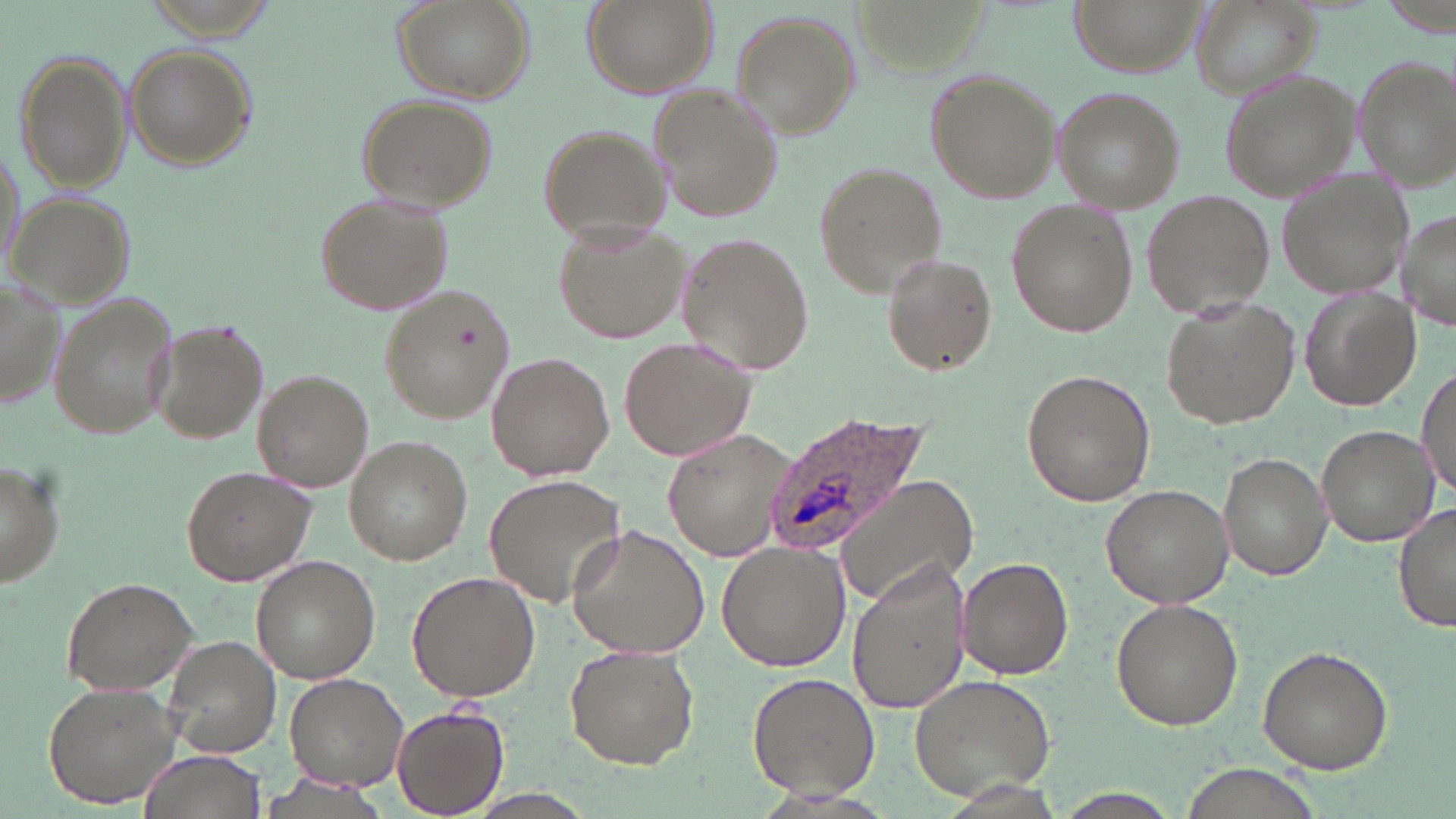
Summary:
  - Coordinate format: approximate bounding boxes as named x1/y1/x2/y2 corners in pixels
  - Plasmodium ovale-infected red blood cell locations: (x1=765, y1=411, x2=934, y2=553)
  - Uninfected red blood cell locations: (x1=391, y1=0, x2=535, y2=103), (x1=580, y1=0, x2=717, y2=99), (x1=1076, y1=0, x2=1205, y2=74), (x1=1189, y1=0, x2=1322, y2=101), (x1=729, y1=10, x2=858, y2=135), (x1=125, y1=43, x2=256, y2=172), (x1=16, y1=52, x2=132, y2=194), (x1=1353, y1=52, x2=1455, y2=188), (x1=922, y1=68, x2=1060, y2=203), (x1=1219, y1=71, x2=1357, y2=202), (x1=651, y1=86, x2=783, y2=223), (x1=1056, y1=89, x2=1182, y2=210), (x1=356, y1=95, x2=497, y2=211), (x1=535, y1=124, x2=669, y2=246), (x1=814, y1=162, x2=947, y2=294), (x1=1278, y1=170, x2=1413, y2=298), (x1=313, y1=189, x2=454, y2=316), (x1=1143, y1=189, x2=1275, y2=320), (x1=7, y1=191, x2=135, y2=310), (x1=1005, y1=199, x2=1136, y2=339), (x1=1398, y1=205, x2=1456, y2=332), (x1=553, y1=219, x2=690, y2=345), (x1=677, y1=233, x2=814, y2=372), (x1=882, y1=253, x2=995, y2=374), (x1=0, y1=276, x2=65, y2=414), (x1=378, y1=283, x2=517, y2=424), (x1=1300, y1=286, x2=1420, y2=411), (x1=48, y1=292, x2=179, y2=441), (x1=1160, y1=298, x2=1298, y2=428), (x1=149, y1=318, x2=270, y2=444), (x1=619, y1=335, x2=755, y2=462), (x1=487, y1=353, x2=615, y2=480), (x1=1416, y1=366, x2=1455, y2=500), (x1=253, y1=368, x2=372, y2=492), (x1=1022, y1=368, x2=1155, y2=506), (x1=1316, y1=424, x2=1435, y2=544), (x1=663, y1=427, x2=794, y2=563), (x1=343, y1=437, x2=473, y2=565), (x1=1218, y1=451, x2=1332, y2=581), (x1=0, y1=458, x2=65, y2=589), (x1=180, y1=465, x2=316, y2=587), (x1=834, y1=473, x2=979, y2=607), (x1=486, y1=475, x2=627, y2=609), (x1=1101, y1=483, x2=1234, y2=608), (x1=1394, y1=500, x2=1454, y2=635), (x1=566, y1=524, x2=710, y2=659), (x1=717, y1=541, x2=849, y2=672), (x1=251, y1=556, x2=380, y2=682), (x1=957, y1=556, x2=1074, y2=679), (x1=847, y1=563, x2=972, y2=715), (x1=407, y1=571, x2=540, y2=702), (x1=60, y1=576, x2=199, y2=695), (x1=1110, y1=598, x2=1242, y2=730), (x1=161, y1=635, x2=281, y2=758), (x1=562, y1=644, x2=698, y2=770), (x1=1255, y1=645, x2=1393, y2=773), (x1=746, y1=672, x2=879, y2=800), (x1=284, y1=673, x2=411, y2=790), (x1=907, y1=673, x2=1058, y2=802), (x1=43, y1=679, x2=187, y2=808), (x1=392, y1=704, x2=508, y2=816), (x1=142, y1=750, x2=262, y2=819), (x1=1175, y1=765, x2=1327, y2=819)
  - Slide-level diagnosis: Plasmodium ovale
  - Image size: 1456×819 pixels
  - Stain: May-Grünwald-Giemsa
  - Modality: optical microscopy
  - Magnification: 1000x
  - Field of view: one of a larger specimen
  - Preparation: thin blood film